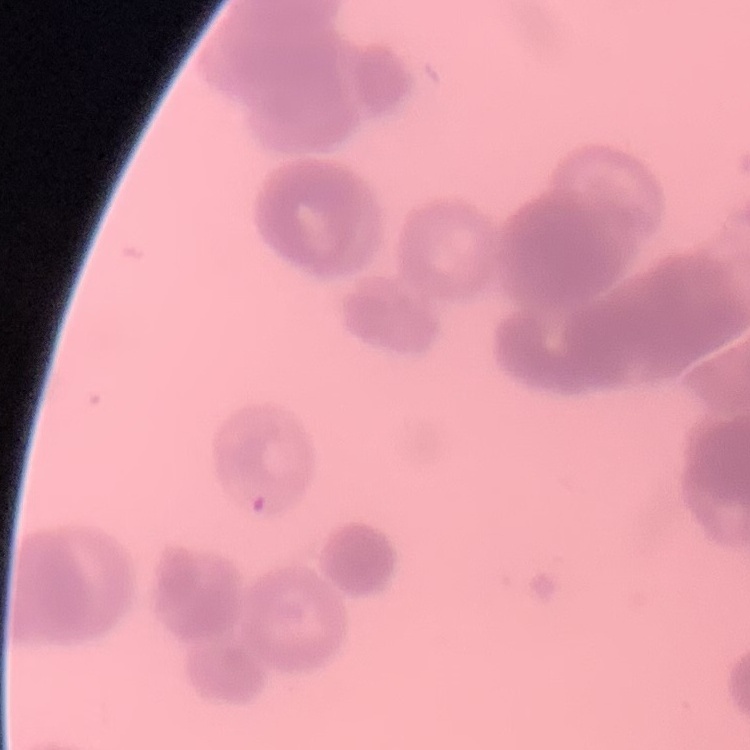
{
  "erythrocyte_morphology": "rouleaux formation",
  "stain": "Field's or Giemsa",
  "preparation": "thin peripheral smear",
  "image_type": "square crop of a larger photomicrograph"
}